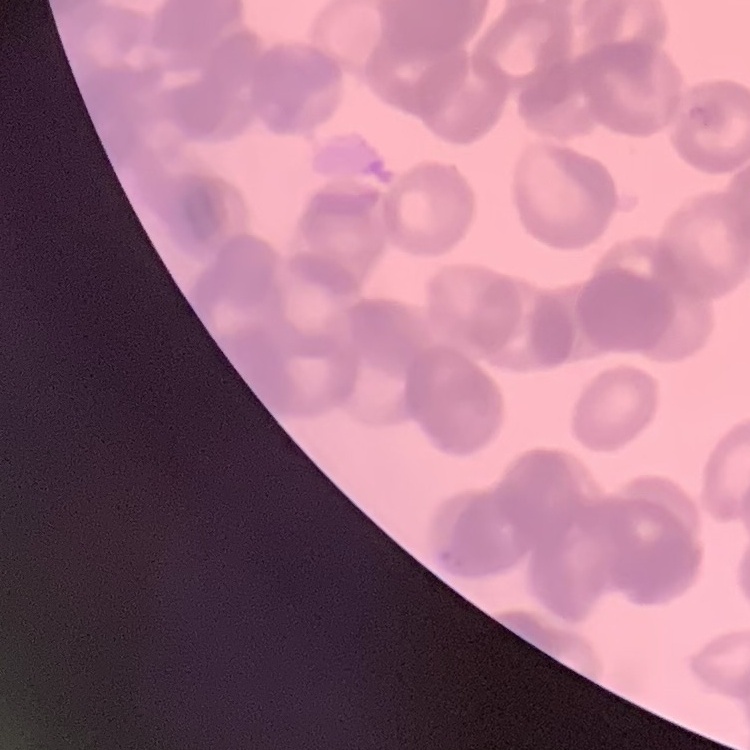
erythrocyte morphology = rouleaux formation
stain = Field's or Giemsa
preparation = thin blood film
image type = one tile cut from a larger photomicrograph